Mark where leukocytes are.
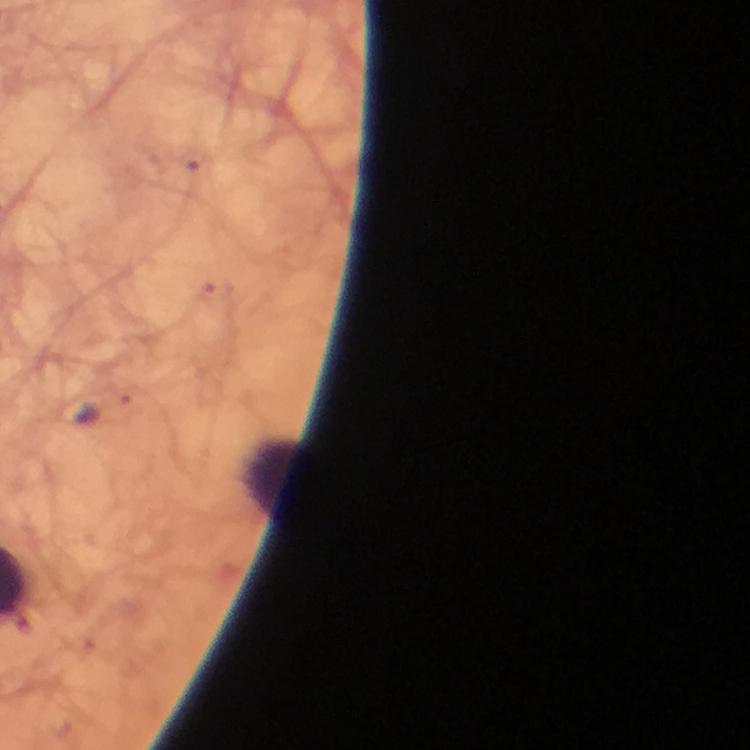
Approximate centers as [x, y] in pixels.
Leukocytes: [276, 476].

{
  "image_size": "750×750 pixels",
  "magnification": "100x",
  "context": "from a malaria diagnostic workup",
  "capture": "smartphone mounted on the microscope",
  "immersion_oil": "used",
  "malaria_parasite_locations": "approximate centers as [x, y] in pixels: [104, 410]",
  "stain": "Giemsa",
  "preparation": "thick smear",
  "cropped_from": "a single field of view"
}